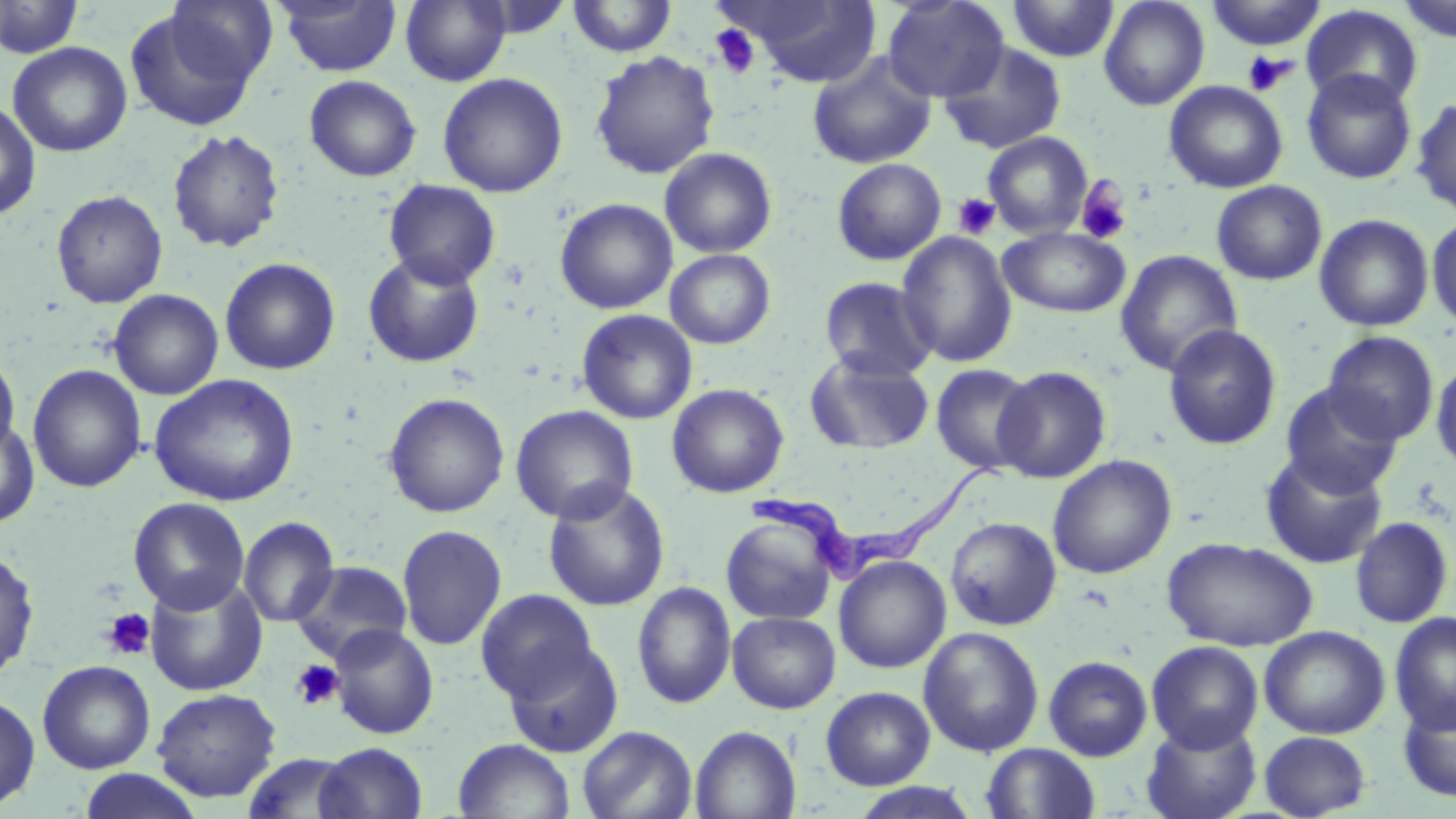

slide-level diagnosis = Trypanosoma brucei
magnification = 1000x
uninfected red blood cell locations = approximate bounding boxes as (x1, y1, x2, y2) in pixels: (276, 0, 403, 76), (401, 0, 511, 86), (469, 0, 575, 39), (728, 0, 882, 86), (882, 0, 1009, 103), (1007, 0, 1119, 62), (1098, 0, 1210, 111), (1205, 0, 1327, 50), (1398, 0, 1455, 43), (1, 1, 85, 60), (567, 1, 678, 58), (165, 2, 279, 88), (1301, 4, 1423, 111), (125, 8, 264, 131), (939, 41, 1067, 154), (7, 42, 132, 157), (590, 51, 720, 179), (806, 51, 937, 170), (1301, 69, 1418, 184), (438, 72, 568, 197), (304, 75, 422, 182), (1164, 80, 1288, 193), (1411, 97, 1456, 216), (0, 100, 41, 221), (167, 129, 285, 253), (982, 132, 1094, 238), (659, 147, 777, 258), (832, 158, 947, 265), (383, 179, 501, 289), (1211, 180, 1327, 285), (51, 190, 168, 308), (555, 197, 678, 314), (1314, 213, 1434, 332), (1427, 214, 1456, 332), (998, 227, 1130, 317), (897, 230, 1017, 368), (665, 249, 776, 349), (1115, 250, 1242, 377), (363, 251, 485, 368), (219, 257, 340, 375), (818, 276, 938, 382), (108, 289, 224, 400), (576, 309, 697, 425), (1165, 324, 1282, 450), (1322, 330, 1439, 446), (0, 350, 20, 460), (804, 350, 933, 456), (1431, 357, 1456, 474), (930, 363, 1038, 475), (28, 364, 146, 493), (992, 366, 1112, 483), (149, 374, 299, 507), (666, 382, 789, 498), (1279, 382, 1405, 498), (383, 392, 510, 518), (510, 404, 639, 524), (0, 418, 40, 528), (1259, 449, 1388, 569), (1048, 454, 1177, 579), (542, 480, 671, 612), (128, 497, 250, 615), (720, 516, 838, 625), (945, 516, 1062, 630), (1350, 516, 1454, 629), (238, 517, 338, 627), (396, 524, 507, 651), (1163, 536, 1319, 651), (0, 549, 39, 682), (833, 555, 952, 673), (290, 560, 413, 663), (145, 575, 267, 695), (632, 582, 736, 709), (476, 588, 599, 703), (727, 611, 840, 714), (1389, 612, 1456, 735), (328, 623, 439, 739), (1259, 626, 1390, 739), (919, 627, 1044, 757), (503, 640, 624, 758), (1146, 640, 1264, 752), (1043, 655, 1153, 762), (37, 660, 155, 774), (820, 686, 935, 790), (151, 688, 282, 802), (1398, 693, 1456, 803), (0, 694, 40, 812), (1141, 717, 1262, 819), (577, 724, 698, 819), (690, 725, 801, 819), (1259, 731, 1371, 817), (453, 738, 576, 819), (314, 742, 429, 819), (981, 743, 1101, 819), (241, 752, 359, 818), (78, 768, 204, 819), (849, 782, 983, 818)
image size = 1456×819 pixels
modality = optical microscopy
Trypanosoma brucei locations = approximate bounding boxes as (x1, y1, x2, y2) in pixels: (750, 461, 1014, 577)
platelet locations = approximate bounding boxes as (x1, y1, x2, y2) in pixels: (710, 24, 761, 79), (1242, 51, 1295, 96), (1074, 175, 1133, 245), (953, 193, 1000, 240), (101, 607, 156, 660), (290, 659, 345, 710)
stain = May-Grünwald-Giemsa
preparation = thin blood film
field of view = single